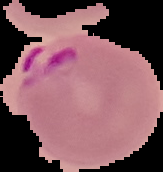
Malaria status: parasitized. Image is 163×172 pixels. Cell region segmented out of the field of view; the surrounding area is masked to black. From a thin blood film.